Evaluate for Plasmodium parasites.
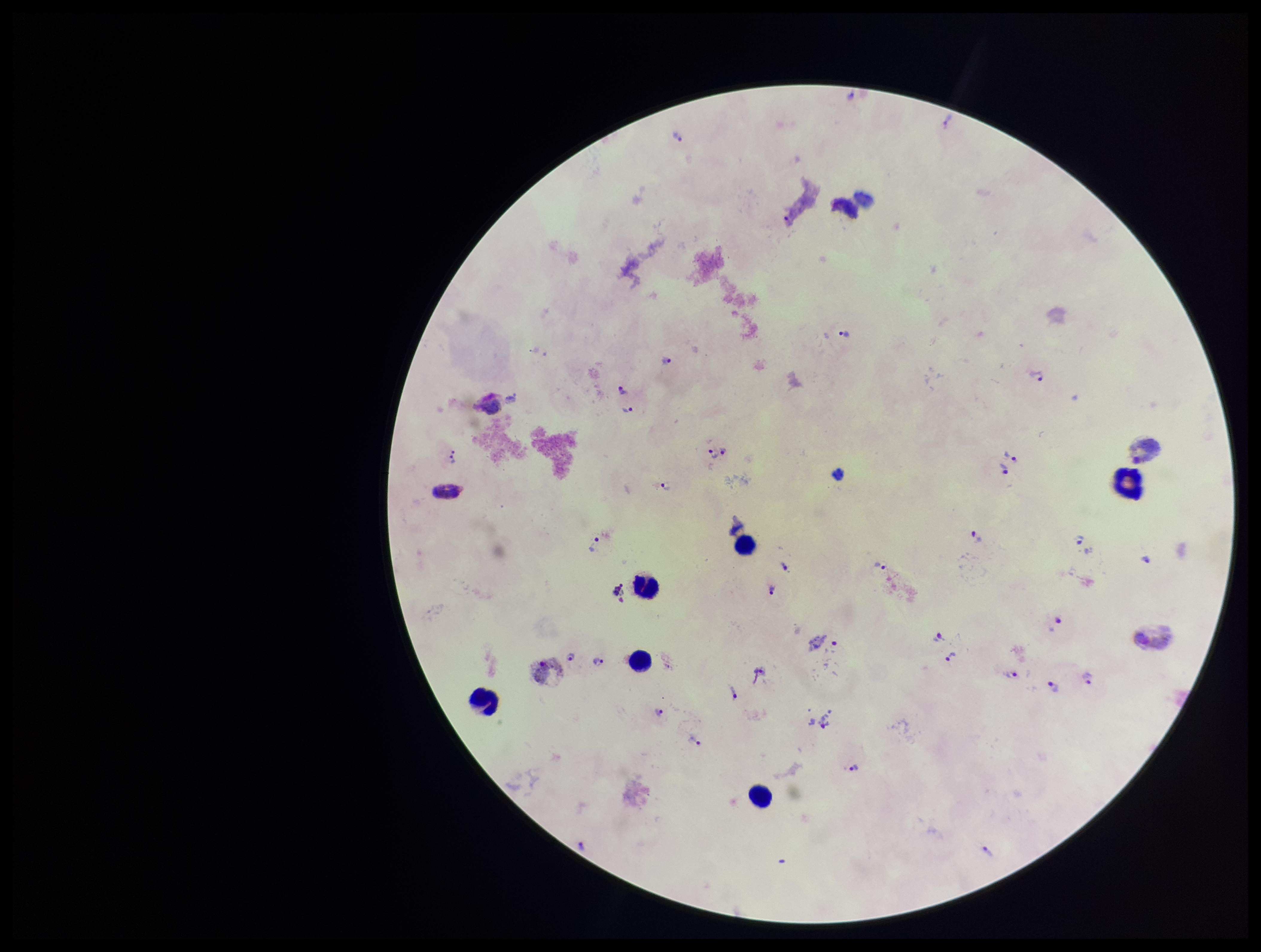

Identified.

parasite count = 32
leukocyte count = 6
preparation = thick
species reported for this patient = Plasmodium vivax
patient malaria status = infected
image size = 1261×952 pixels
stain = Giemsa
capture = smartphone photograph through the microscope eyepiece
field of view = single